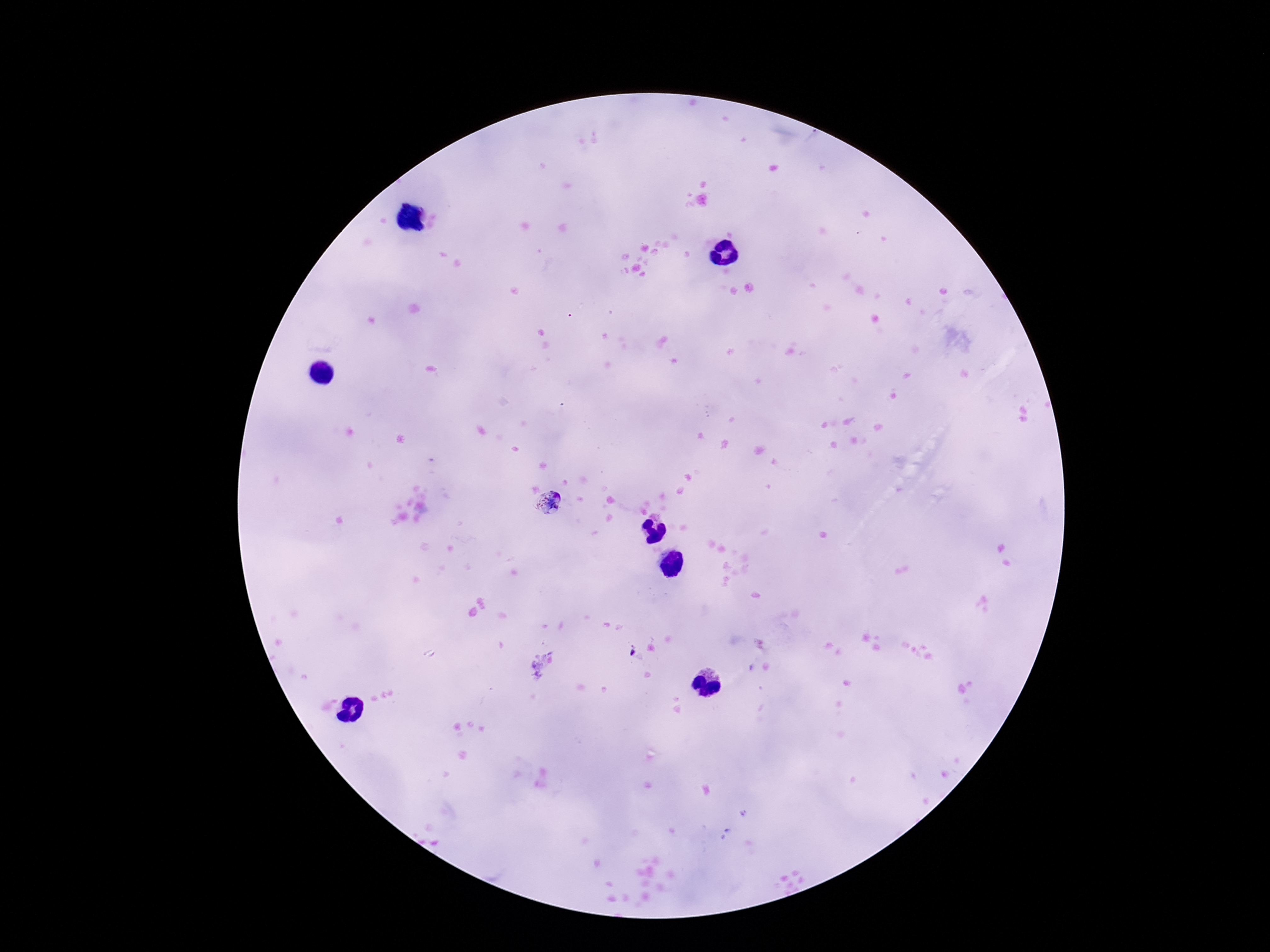
Approximate centers as (x, y) in pixels.
Summary:
  - Plasmodium parasite locations: (550, 505), (632, 650)
  - Preparation: thick blood film
  - Capture: smartphone camera through the microscope eyepiece
  - Stain: Giemsa
  - Field of view: one from this slide
  - Image size: 1270×952 pixels
  - Patient malaria status: infected
  - Magnification: 100x